Assess the morphology of the erythrocytes.
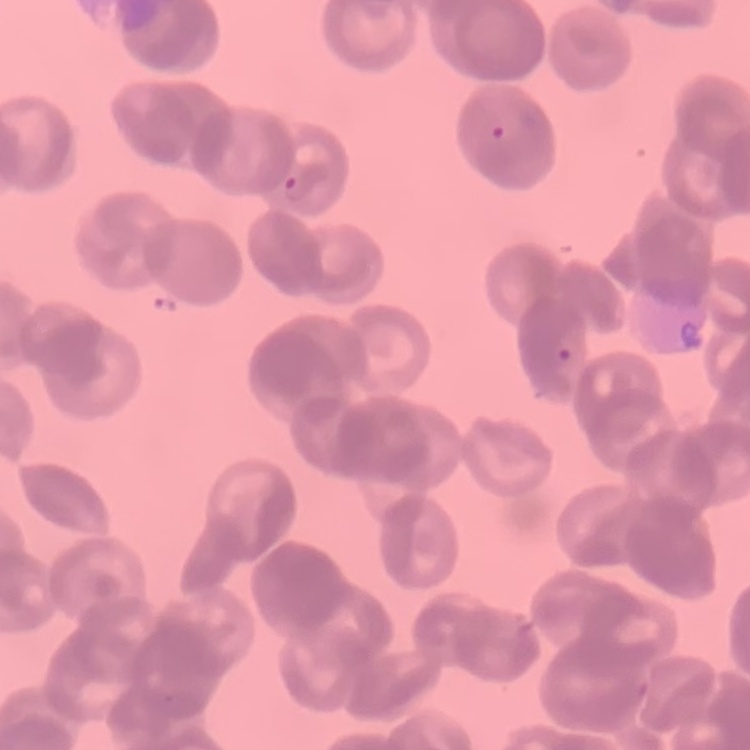

They show rouleaux formation.

image type = square crop of a larger photomicrograph
preparation = thin blood smear
stain = Field's or Giemsa